Assess the morphology of the erythrocytes.
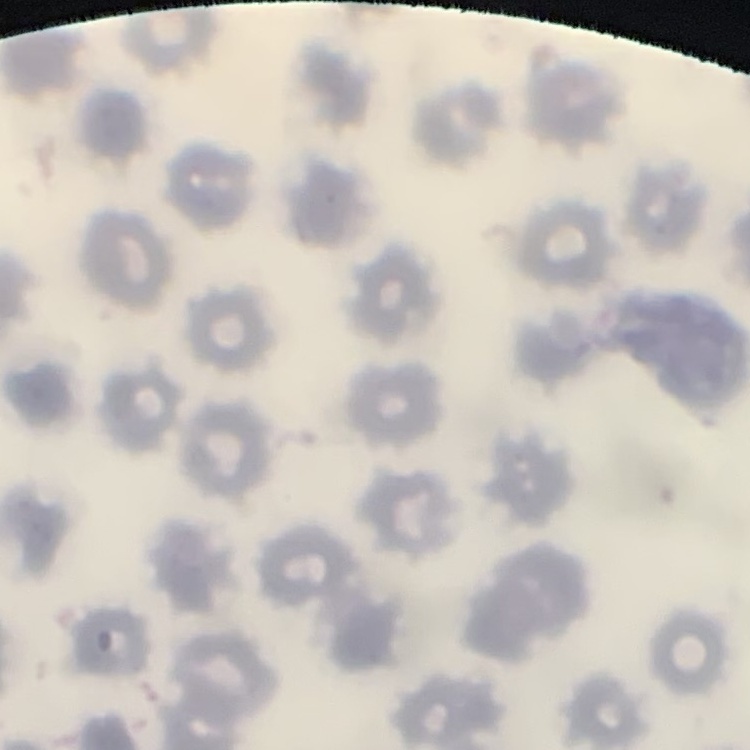

No rouleaux formation.

Summary:
  - Image type: one tile cut from a larger photomicrograph
  - Stain: Field's or Giemsa
  - Preparation: thin peripheral smear